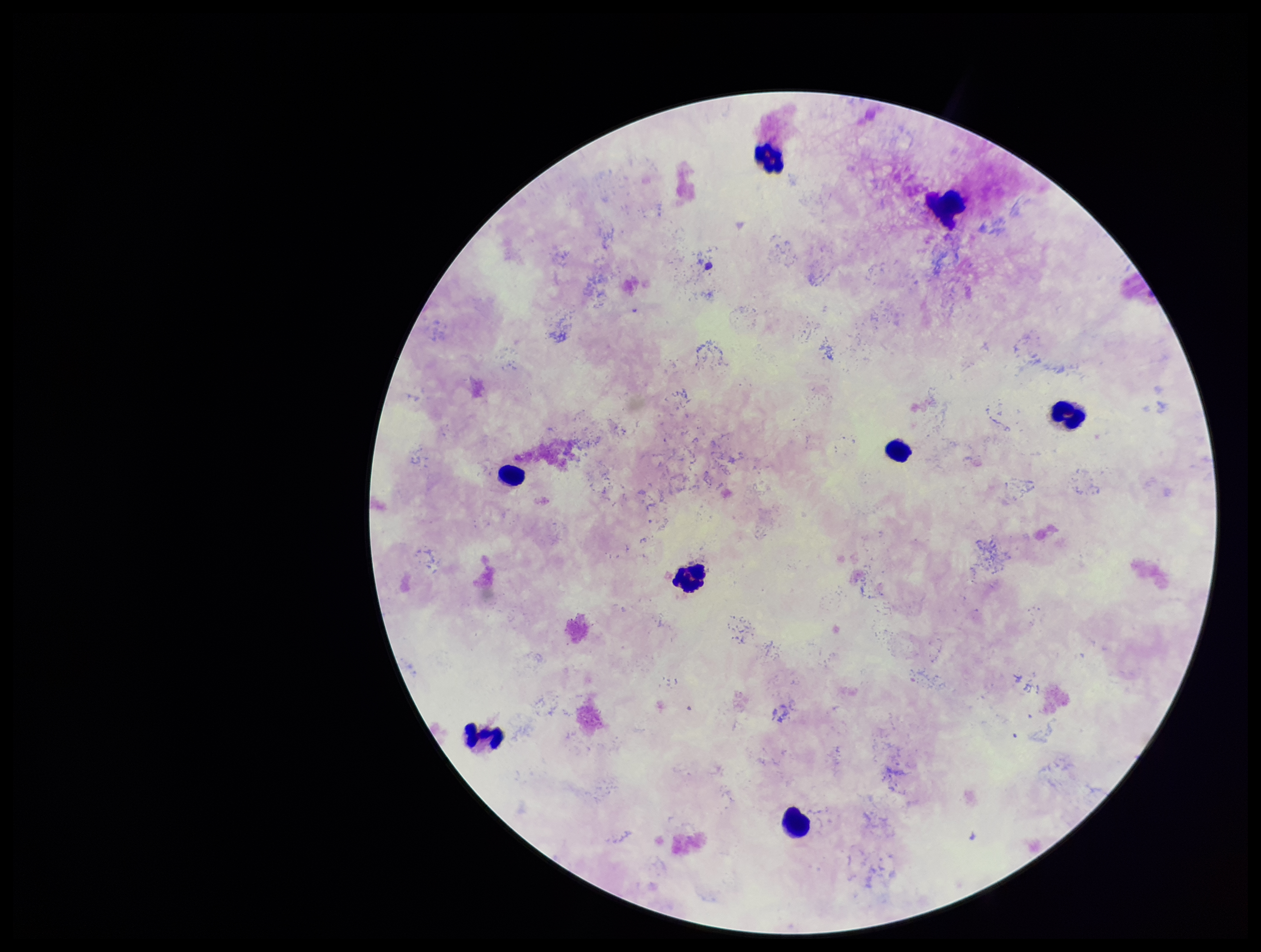

Summary:
  - Patient malaria status: positive
  - Preparation: thick blood smear
  - Plasmodium parasites: none detected
  - Leukocyte count: 8
  - Stain: Giemsa
  - Field of view: one from this slide
  - Parasite count: 0
  - Capture: smartphone photograph through the microscope eyepiece
  - Image size: 1261×952 pixels
  - Species reported for this patient: Plasmodium falciparum